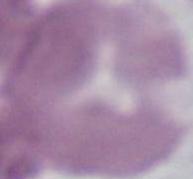

magnification = 1000x
modality = photomicrograph
identification = red blood cell